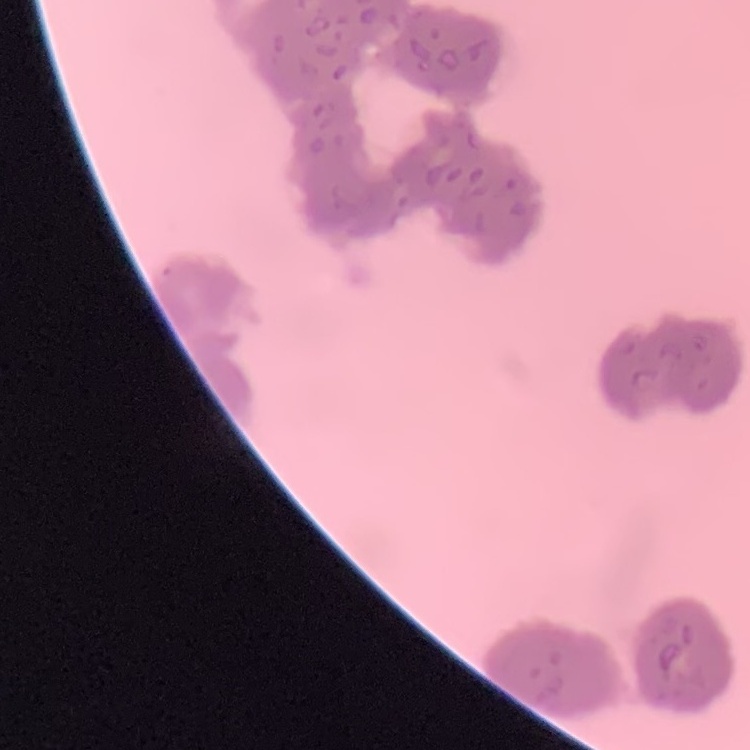

{
  "red_blood_cell_morphology": "rouleaux formation",
  "stain": "Field's or Giemsa",
  "image_type": "one tile cut from a larger photomicrograph",
  "preparation": "thin blood film"
}